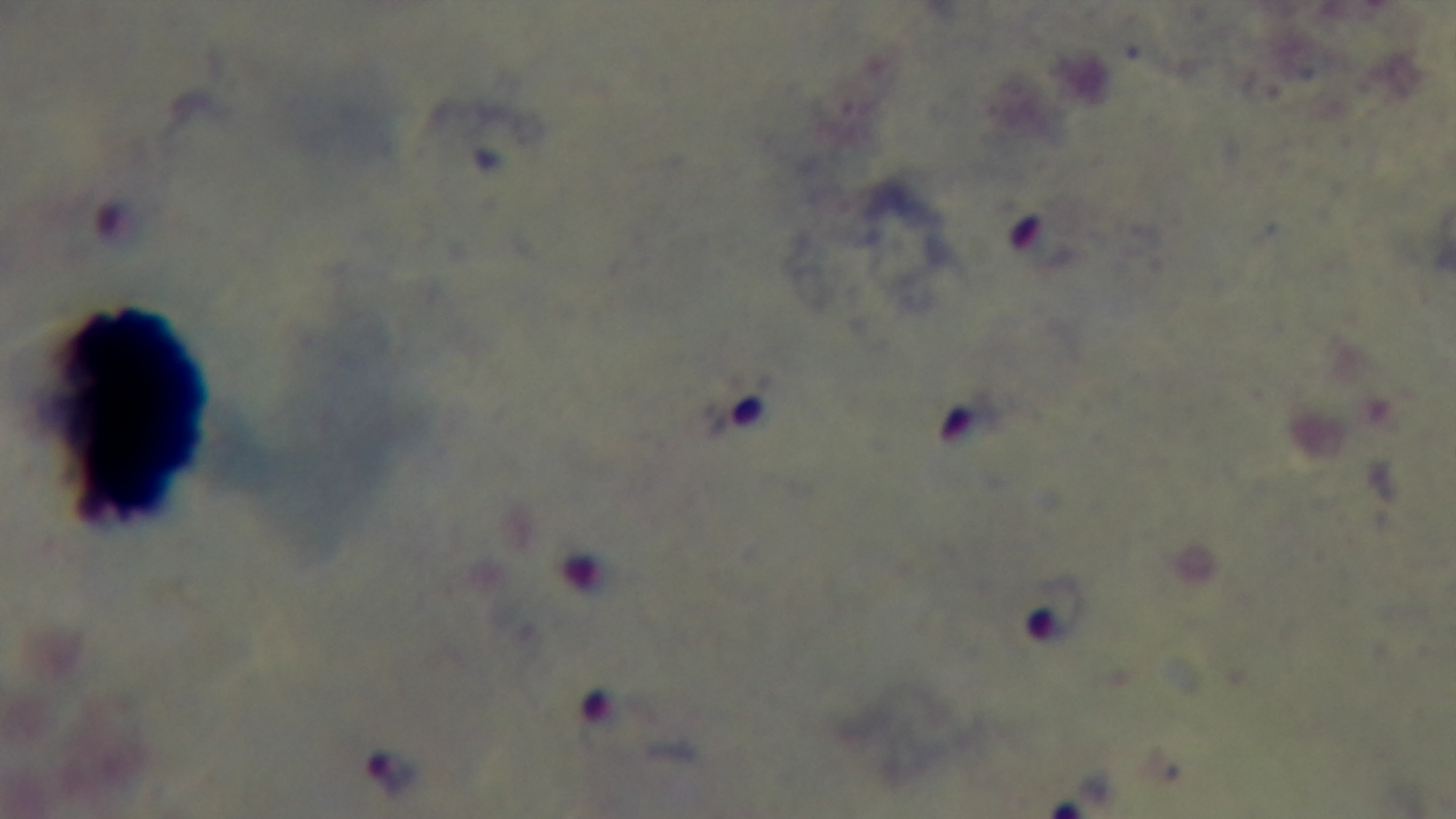 Preparation: thick smear. Oil-immersion objective, 100x. Single field of view. Malaria status: positive. Mounted 4K digital camera. Giemsa stain. Light microscopy.